Assess this cell for malaria.
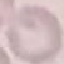

It is uninfected.

Giemsa-stained preparation. Automatically extracted cell patch, resized to 64 × 64 pixels. Photographed with a smartphone camera at the microscope eyepiece. Thin blood film.